Identify the cell.
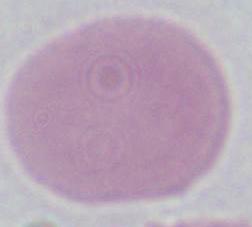
An erythrocyte.

Summary:
  - Magnification: 1000x
  - Modality: micrograph